Assess this cell for malaria.
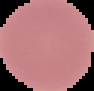
It is uninfected.

Summary:
  - Image size: 94×91 pixels
  - Preparation: thin blood smear
  - Image type: cell region segmented out of the field of view; surrounding area masked to black